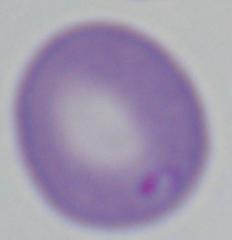
identification = Babesia
modality = photomicrograph
magnification = 1000x